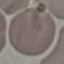

malaria status = uninfected
image type = automatically extracted cell patch, resized to 64 × 64 pixels
capture = smartphone through the microscope eyepiece
stain = Giemsa
preparation = thin smear